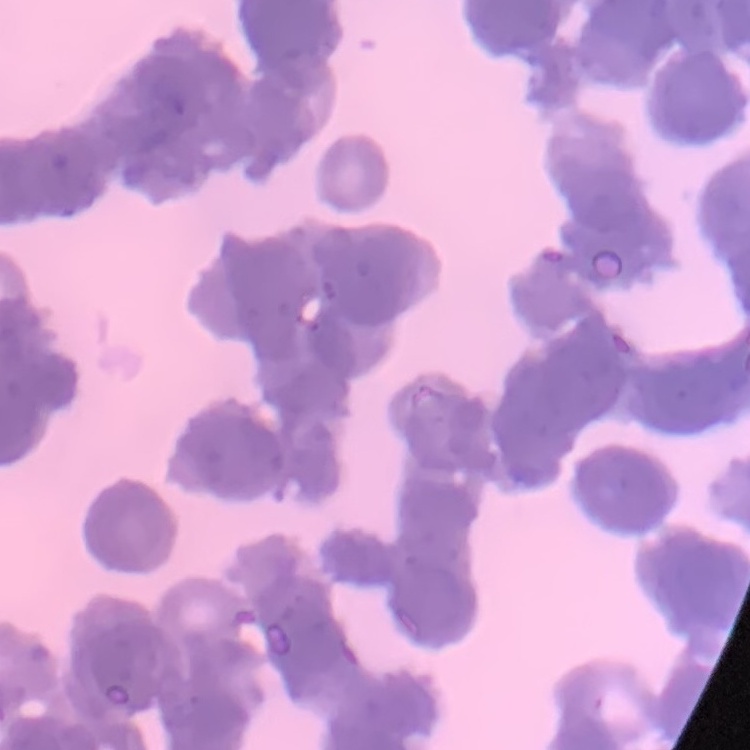
erythrocyte morphology = rouleaux formation
image type = square crop of a larger photomicrograph
stain = Field's or Giemsa
preparation = thin peripheral smear